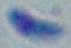

Summary:
  - Magnification: 1000x
  - Modality: photomicrograph
  - Identification: Toxoplasma gondii